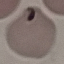
result = malaria parasites detected
stain = Giemsa
capture = smartphone camera at the microscope eyepiece
image type = automatically extracted cell patch, resized to 64 × 64 pixels
preparation = thin blood film